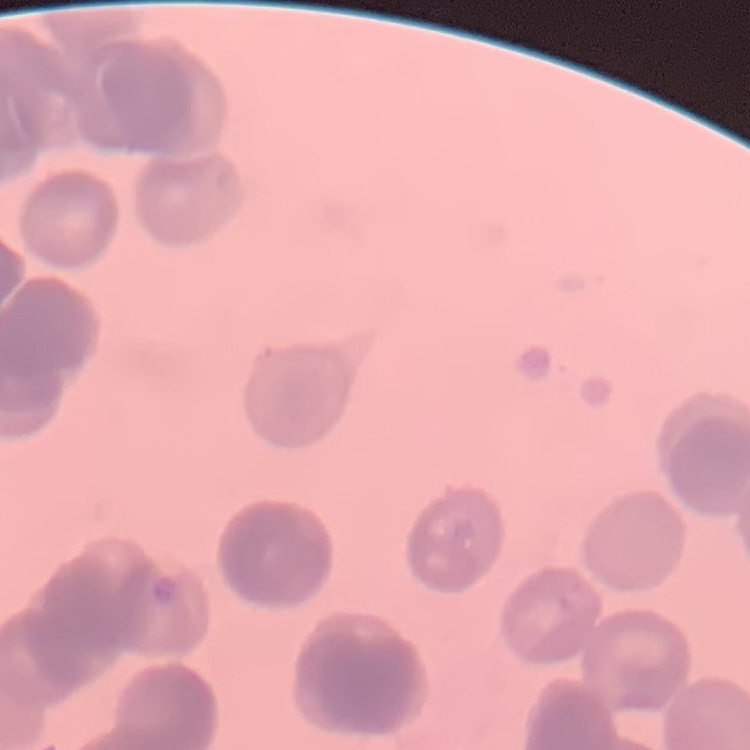

Summary:
  - Red blood cell morphology: rouleaux formation
  - Stain: Field's or Giemsa
  - Preparation: thin blood film
  - Image type: one tile cut from a larger photomicrograph